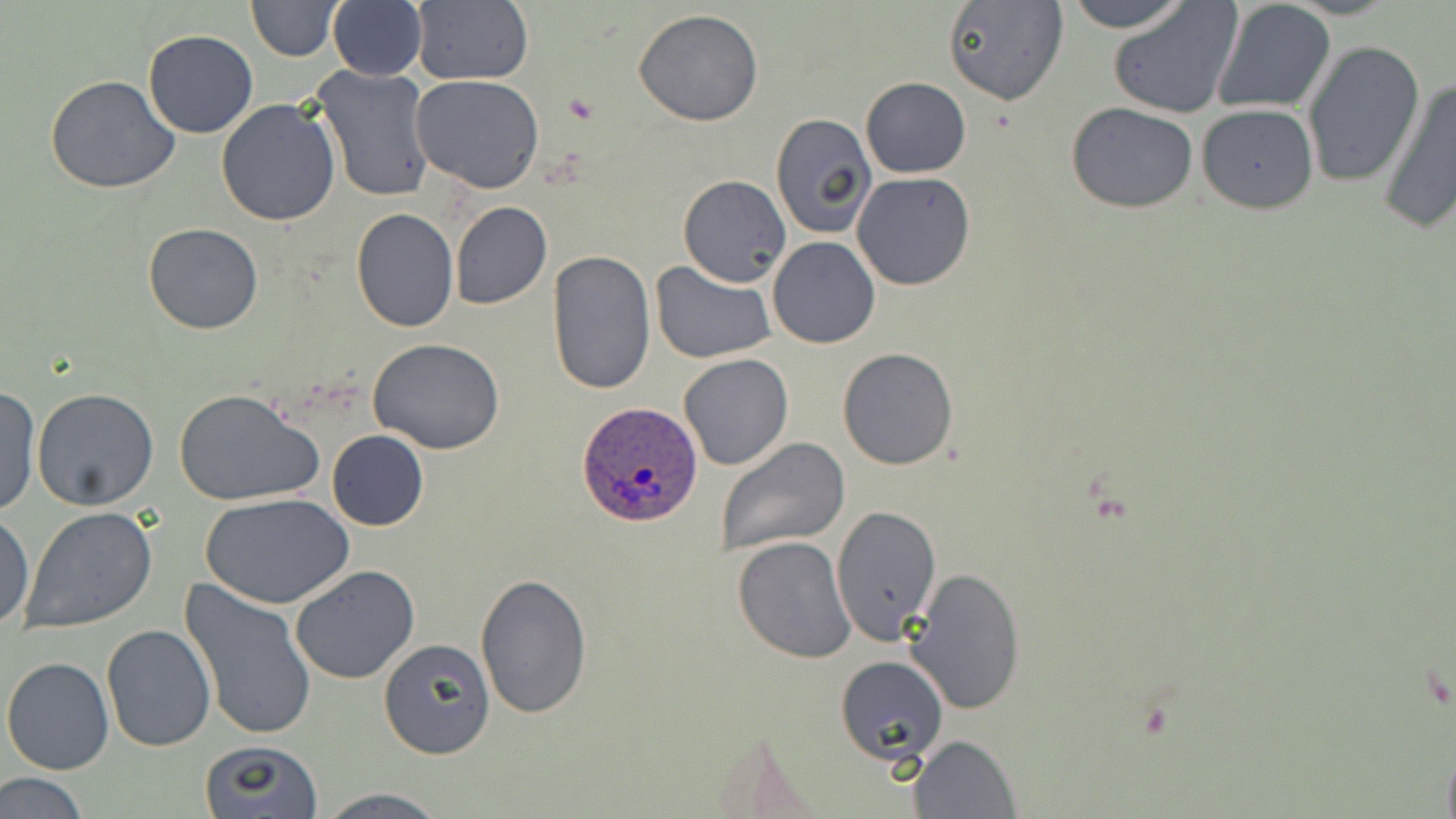
slide_level_diagnosis: Plasmodium ovale
magnification: 1000x
modality: light microscopy
field_of_view: single
image_size: 1456×819 pixels
uninfected_red_blood_cell_locations: 'approximate bounding boxes as named x1/y1/x2/y2 corners in pixels: (x1=246, y1=0, x2=342, y2=60), (x1=1062, y1=0, x2=1193, y2=33), (x1=408, y1=1, x2=534, y2=87), (x1=942, y1=1, x2=1069, y2=105), (x1=1210, y1=1, x2=1337, y2=115), (x1=327, y1=2, x2=427, y2=80), (x1=1107, y1=2, x2=1242, y2=118), (x1=633, y1=9, x2=764, y2=126), (x1=143, y1=30, x2=257, y2=138), (x1=1302, y1=40, x2=1424, y2=187), (x1=311, y1=63, x2=435, y2=203), (x1=46, y1=74, x2=180, y2=194), (x1=412, y1=74, x2=545, y2=194), (x1=860, y1=77, x2=970, y2=179), (x1=1379, y1=78, x2=1456, y2=234), (x1=216, y1=99, x2=341, y2=226), (x1=1066, y1=102, x2=1199, y2=214), (x1=1196, y1=103, x2=1319, y2=213), (x1=769, y1=113, x2=876, y2=238), (x1=851, y1=171, x2=978, y2=291), (x1=677, y1=175, x2=791, y2=287), (x1=450, y1=201, x2=551, y2=309), (x1=351, y1=208, x2=458, y2=332), (x1=144, y1=222, x2=263, y2=334), (x1=767, y1=237, x2=880, y2=349), (x1=546, y1=251, x2=657, y2=398), (x1=651, y1=261, x2=777, y2=363), (x1=368, y1=337, x2=507, y2=454), (x1=837, y1=347, x2=959, y2=469), (x1=679, y1=354, x2=793, y2=472), (x1=0, y1=388, x2=39, y2=517), (x1=32, y1=388, x2=159, y2=510), (x1=173, y1=388, x2=325, y2=507), (x1=326, y1=431, x2=429, y2=530), (x1=715, y1=437, x2=850, y2=558), (x1=203, y1=494, x2=354, y2=609), (x1=834, y1=504, x2=943, y2=648), (x1=19, y1=505, x2=158, y2=634), (x1=0, y1=509, x2=35, y2=632), (x1=733, y1=536, x2=855, y2=662), (x1=290, y1=564, x2=420, y2=684), (x1=903, y1=565, x2=1028, y2=713), (x1=474, y1=573, x2=593, y2=720), (x1=177, y1=580, x2=318, y2=743), (x1=100, y1=625, x2=215, y2=751), (x1=377, y1=635, x2=496, y2=760), (x1=2, y1=655, x2=115, y2=774), (x1=835, y1=656, x2=949, y2=767), (x1=909, y1=734, x2=1020, y2=818), (x1=196, y1=739, x2=326, y2=819), (x1=2, y1=773, x2=90, y2=818), (x1=316, y1=789, x2=450, y2=819)'
preparation: thin blood smear
plasmodium_ovale_infected_red_blood_cell_locations: 'approximate bounding boxes as named x1/y1/x2/y2 corners in pixels: (x1=577, y1=402, x2=703, y2=529)'
stain: May-Grünwald-Giemsa